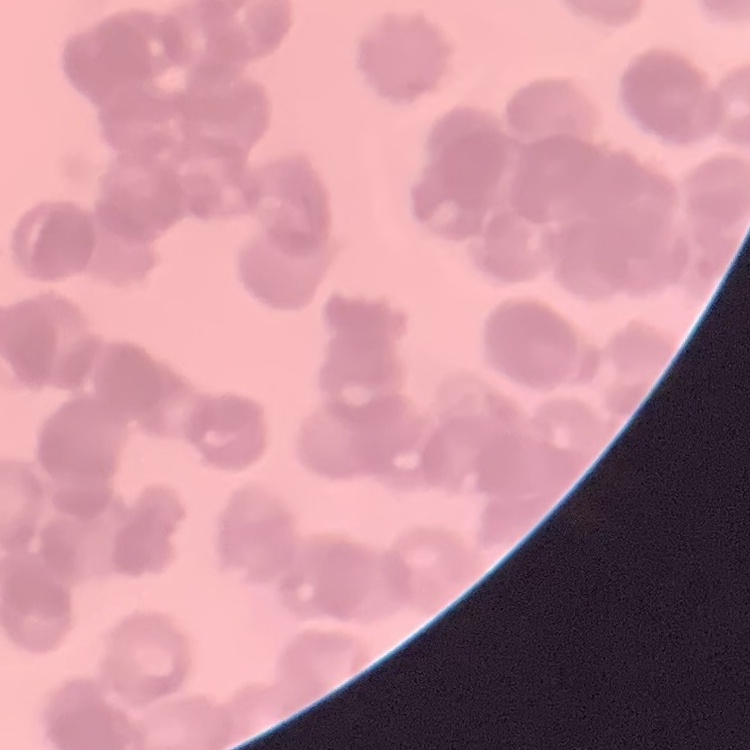

erythrocyte morphology = rouleaux formation
preparation = thin peripheral smear
image type = one tile cut from a larger photomicrograph
stain = Field's or Giemsa